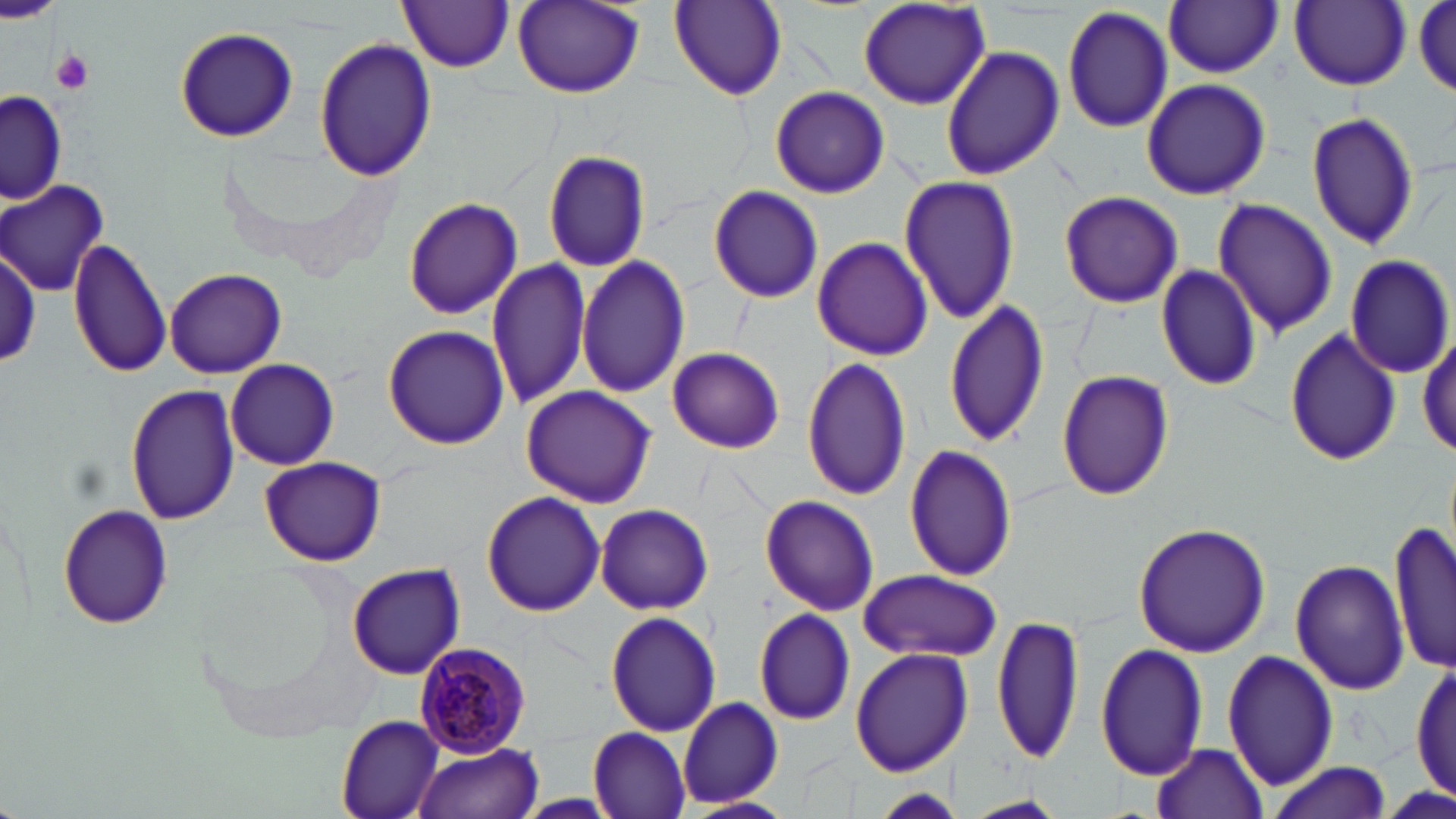
Summary:
  - Coordinate format: approximate bounding boxes as (x1, y1, x2, y2) in pixels
  - Plasmodium malariae-infected red blood cell locations: (410, 642, 533, 758)
  - Uninfected red blood cell locations: (399, 0, 515, 73), (0, 1, 63, 21), (512, 1, 645, 99), (668, 1, 783, 102), (856, 1, 992, 109), (1165, 1, 1282, 78), (1289, 1, 1410, 90), (1414, 1, 1455, 97), (1060, 4, 1174, 135), (174, 28, 298, 142), (312, 36, 436, 184), (939, 46, 1065, 181), (1141, 78, 1271, 201), (770, 86, 889, 198), (2, 88, 67, 205), (1305, 110, 1417, 253), (542, 150, 651, 272), (897, 174, 1020, 326), (0, 180, 110, 295), (708, 185, 824, 304), (1059, 190, 1183, 309), (404, 197, 522, 320), (1210, 197, 1339, 337), (67, 236, 172, 379), (812, 237, 935, 361), (0, 239, 43, 370), (1345, 253, 1454, 377), (577, 255, 688, 397), (487, 258, 593, 413), (1154, 263, 1263, 392), (164, 268, 288, 378), (943, 299, 1051, 448), (384, 324, 510, 449), (1282, 325, 1401, 468), (1417, 333, 1454, 458), (667, 346, 785, 455), (802, 355, 912, 503), (226, 359, 339, 469), (1056, 368, 1175, 502), (125, 382, 238, 525), (520, 384, 659, 507), (903, 444, 1018, 581), (259, 455, 385, 566), (481, 490, 605, 616), (760, 495, 880, 615), (595, 502, 715, 614), (57, 503, 174, 628), (1390, 518, 1455, 674), (1132, 523, 1272, 658), (1291, 557, 1410, 696), (346, 562, 466, 680), (859, 568, 1003, 661), (752, 607, 855, 726), (605, 610, 722, 735), (992, 613, 1082, 767), (1096, 642, 1209, 780), (850, 646, 973, 776), (1224, 649, 1339, 791), (1412, 657, 1455, 808), (678, 696, 783, 807), (336, 715, 444, 819), (588, 728, 689, 817), (1152, 741, 1269, 817), (414, 743, 544, 819), (1262, 762, 1390, 819), (957, 796, 1070, 818)
  - Platelet locations: (50, 49, 94, 94)
  - Slide-level diagnosis: Plasmodium malariae
  - Modality: light microscopy
  - Magnification: 1000x
  - Image size: 1456×819 pixels
  - Stain: May-Grünwald-Giemsa
  - Field of view: one of a larger specimen
  - Preparation: thin blood film